Give the extent of all Plasmodium falciparum-infected red blood cells.
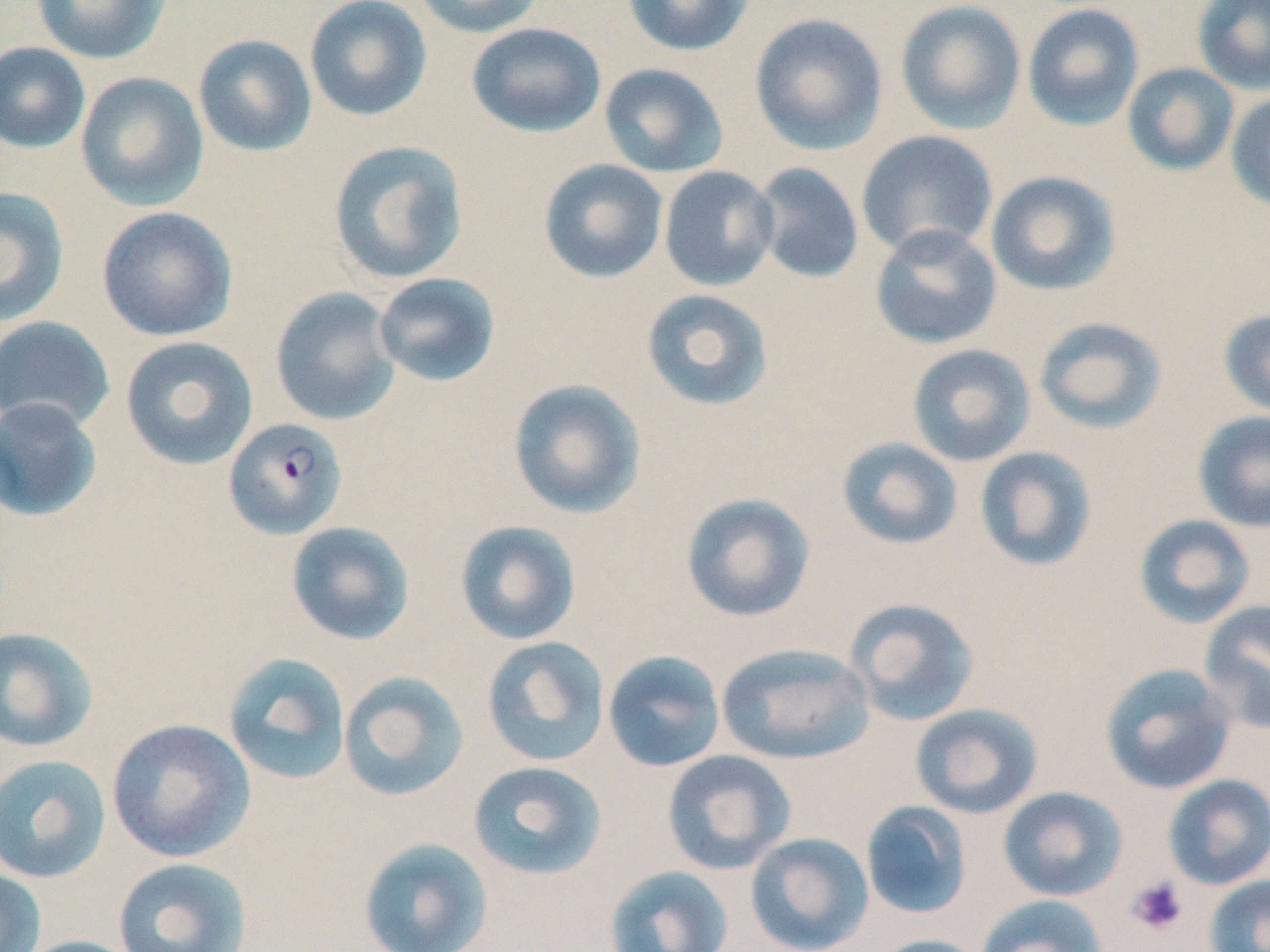

Approximate bounding boxes as (x1, y1, x2, y2) in pixels.
Plasmodium falciparum-infected red blood cells: (223, 418, 348, 541).

Summary:
  - Uninfected red blood cell locations: (30, 0, 171, 65), (304, 0, 432, 122), (410, 0, 546, 38), (622, 0, 756, 57), (895, 0, 1027, 135), (1191, 0, 1270, 96), (1022, 3, 1145, 132), (749, 13, 889, 155), (466, 22, 606, 138), (193, 33, 318, 157), (0, 41, 91, 154), (599, 63, 729, 178), (1122, 63, 1239, 176), (75, 71, 209, 211), (1225, 90, 1270, 213), (855, 129, 999, 259), (327, 139, 469, 285), (538, 159, 669, 283), (751, 162, 864, 284), (658, 166, 779, 291), (985, 170, 1121, 296), (0, 186, 69, 327), (96, 206, 238, 342), (869, 223, 1003, 350), (373, 272, 501, 387), (269, 287, 402, 426), (640, 288, 774, 411), (1218, 308, 1270, 419), (0, 316, 116, 433), (1033, 316, 1167, 435), (120, 335, 258, 470), (906, 343, 1036, 467), (507, 378, 647, 519), (0, 397, 103, 522), (1192, 410, 1270, 532), (835, 437, 964, 551), (974, 446, 1098, 572), (679, 492, 817, 623), (1133, 513, 1256, 629), (454, 520, 582, 646), (285, 521, 416, 645), (844, 597, 980, 726), (1199, 600, 1270, 733), (0, 627, 99, 753), (481, 636, 610, 767), (716, 642, 875, 765), (601, 649, 727, 773), (223, 652, 351, 785), (1100, 663, 1238, 794), (337, 670, 470, 802), (909, 703, 1044, 819), (106, 718, 256, 862), (661, 749, 795, 875), (0, 754, 112, 884), (467, 760, 607, 880), (1162, 774, 1270, 890), (997, 786, 1128, 902), (861, 801, 972, 920), (745, 832, 874, 952), (358, 836, 493, 952), (112, 857, 252, 952), (604, 864, 734, 952), (0, 866, 46, 952), (1205, 874, 1270, 952), (977, 894, 1110, 952), (869, 934, 991, 952), (14, 936, 146, 952)
  - Platelet locations: (1125, 875, 1189, 936)
  - Slide-level diagnosis: Plasmodium falciparum
  - Modality: optical microscopy
  - Magnification: 1000x
  - Field of view: single
  - Image size: 1270×952 pixels
  - Preparation: thin blood film
  - Stain: May-Grünwald-Giemsa